Assess this cell for malaria.
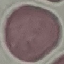
Uninfected.

Summary:
  - Image type: automatically extracted cell patch, resized to 64 × 64 pixels
  - Preparation: thin blood film
  - Capture: smartphone camera at the microscope eyepiece
  - Stain: Giemsa